Give the extent of all white blood cells.
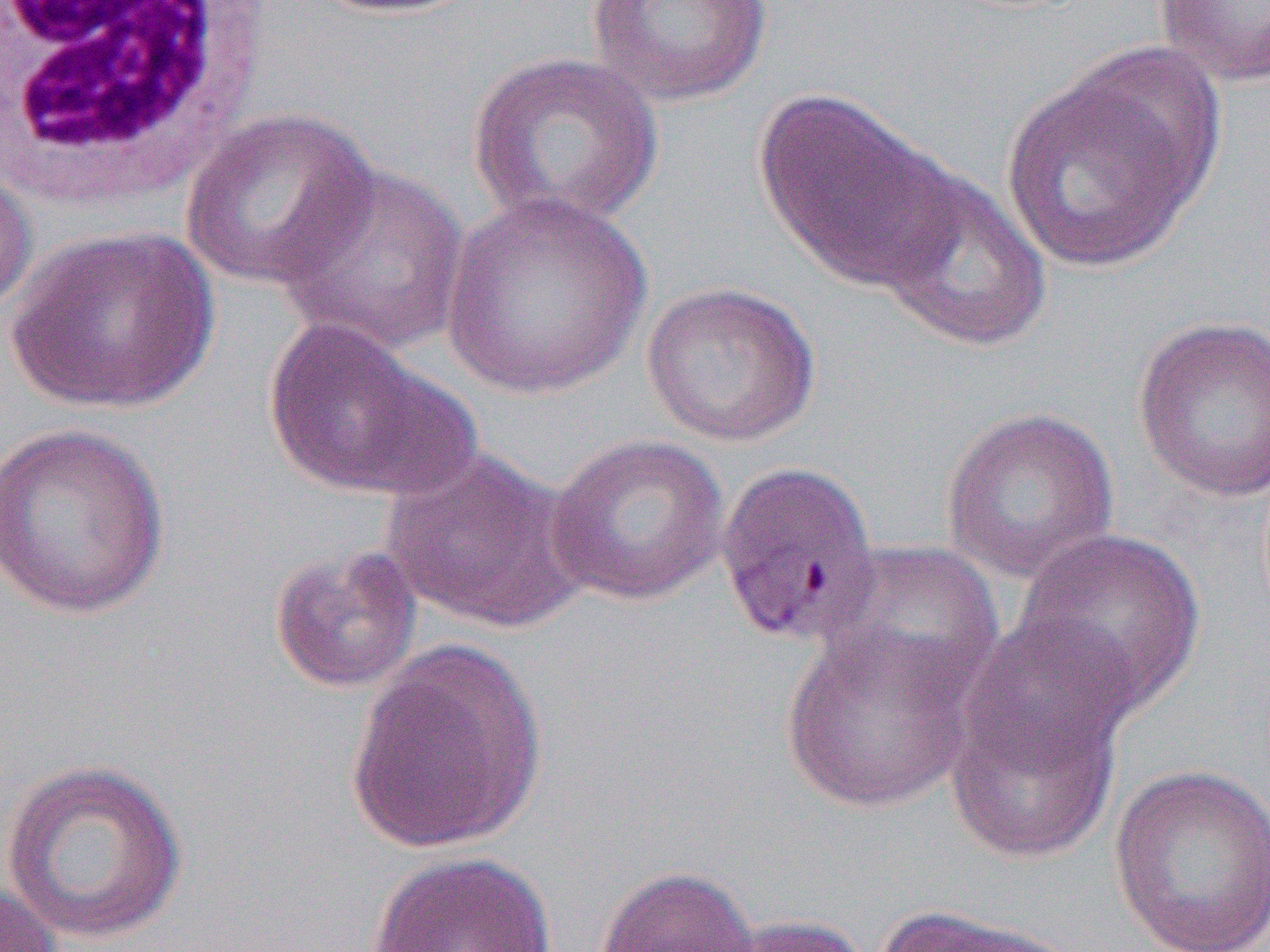
Approximate bounding boxes as [x1, y1, x2, y2] in pixels.
White blood cells: [0, 0, 276, 205].

Summary:
  - Uninfected red blood cell locations: [306, 0, 479, 18], [1151, 0, 1270, 89], [584, 1, 775, 108], [466, 51, 665, 233], [1000, 59, 1215, 276], [753, 89, 961, 294], [180, 107, 377, 291], [272, 160, 470, 355], [0, 162, 38, 321], [873, 167, 1053, 353], [441, 190, 653, 399], [4, 226, 221, 415], [639, 280, 822, 448], [1132, 314, 1270, 503], [262, 316, 467, 500], [940, 405, 1120, 584], [0, 422, 171, 619], [545, 434, 731, 607], [379, 448, 591, 635], [1011, 527, 1207, 717], [819, 540, 1003, 705], [269, 543, 423, 695], [780, 623, 980, 814], [946, 630, 1129, 866], [346, 639, 548, 856], [0, 758, 189, 945], [1107, 765, 1270, 951], [366, 850, 557, 952], [593, 864, 761, 952], [0, 879, 64, 951], [873, 905, 1078, 952], [714, 915, 872, 952]
  - Slide-level diagnosis: Plasmodium vivax
  - Magnification: 1000x
  - Image size: 1270×952 pixels
  - Field of view: single
  - Modality: optical microscopy
  - Preparation: thin blood smear